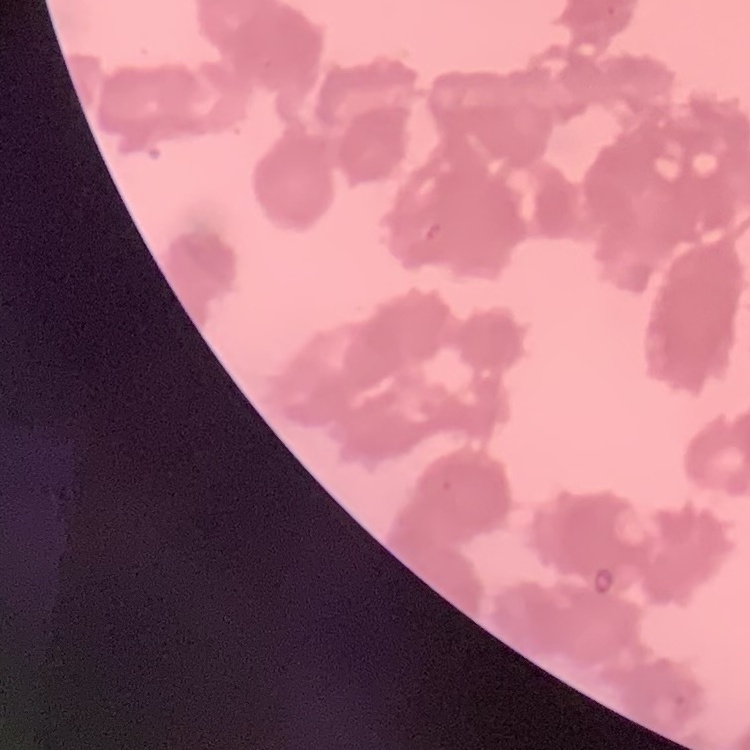

Summary:
  - Red blood cell morphology: rouleaux formation
  - Image type: one tile cut from a larger photomicrograph
  - Preparation: thin blood smear
  - Stain: Field's or Giemsa